Locate every malaria parasite.
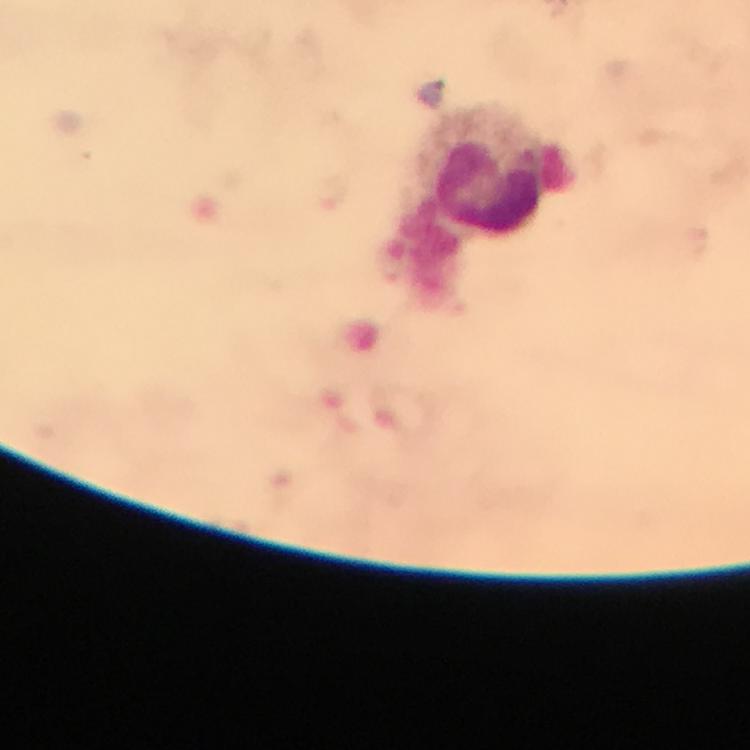
No malaria parasites seen.

Approximate centers as [x, y] in pixels.
Summary:
  - Leukocyte locations: [484, 174]
  - Immersion oil: used
  - Magnification: 100x
  - Preparation: thick blood film
  - Capture: smartphone photograph through a microscope
  - Stain: Giemsa
  - Cropped from: one field of view
  - Image size: 750×750 pixels
  - Context: from a malaria diagnostic workup